Report the malaria status of this cell.
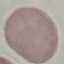
Uninfected.

Summary:
  - Image type: automatically extracted cell patch, resized to 64 × 64 pixels
  - Stain: Giemsa
  - Preparation: thin smear
  - Capture: smartphone camera at the microscope eyepiece